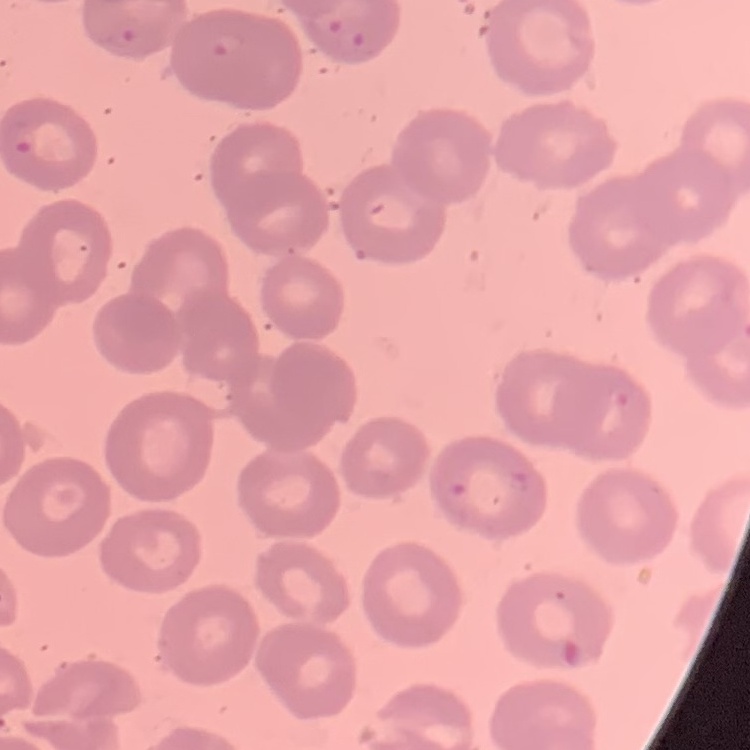

The erythrocytes show no rouleaux formation. Field's or Giemsa stain. Thin blood smear. One tile cut from a larger photomicrograph.